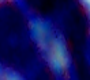

magnification: 1000x
modality: micrograph
identification: leukocyte